Classify this cell by malaria status.
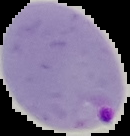

Parasitized.

Summary:
  - Preparation: thin blood smear
  - Image type: segmented cell region with the area outside set to black
  - Image size: 130×136 pixels